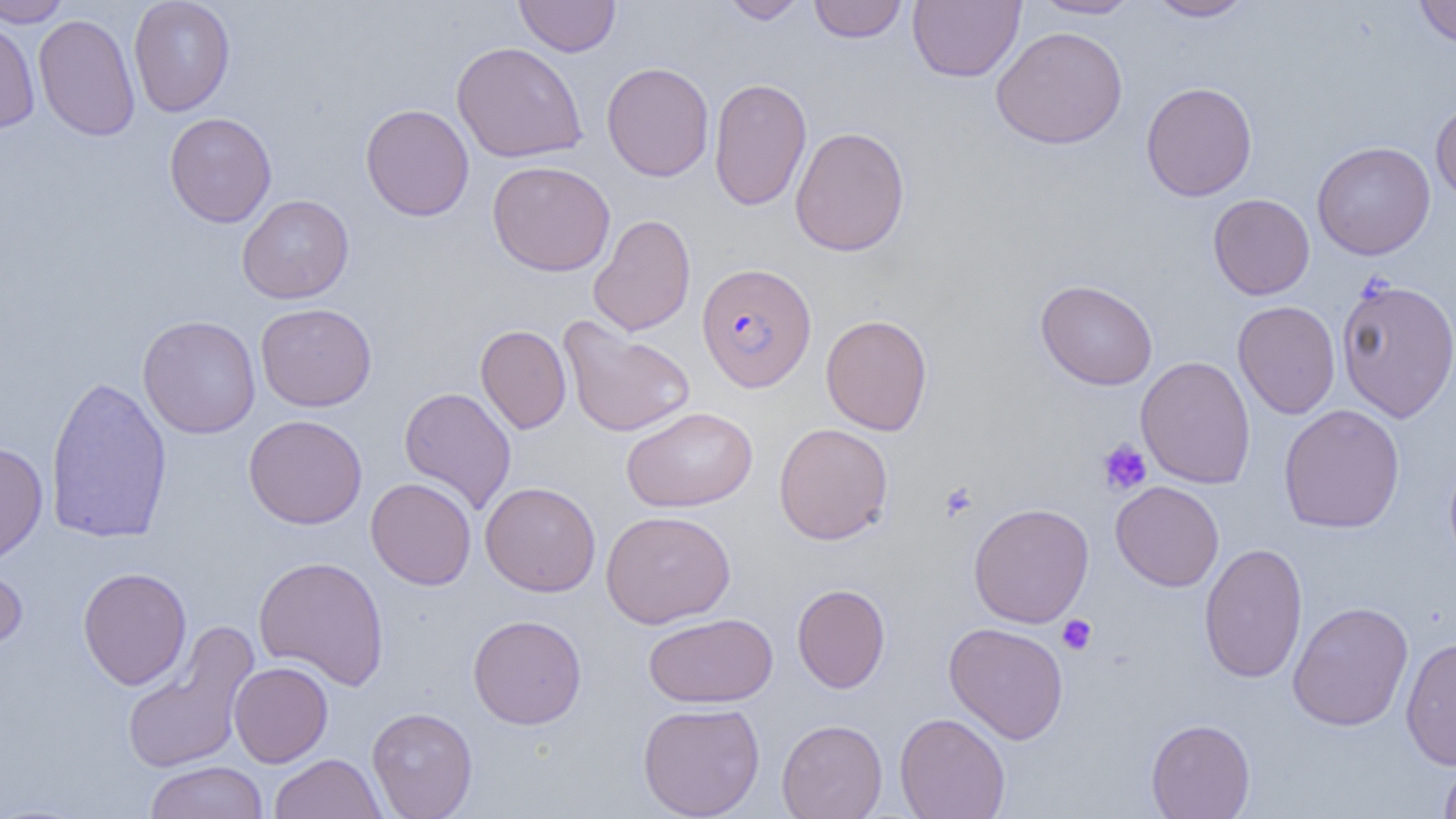

Summary:
  - Coordinate format: approximate bounding boxes as (x1,y1)-(x2,y2) corner pairs in pixels
  - Uninfected red blood cell locations: (0,0)-(72,28), (128,0)-(235,117), (514,0)-(620,57), (719,0)-(809,24), (808,0)-(907,43), (908,0)-(1025,82), (1029,0)-(1140,19), (1145,0)-(1257,21), (1413,0)-(1456,48), (33,13)-(141,142), (0,15)-(40,133), (991,26)-(1128,149), (451,41)-(588,163), (601,62)-(714,181), (709,77)-(811,210), (1140,81)-(1257,201), (1430,99)-(1456,204), (360,103)-(474,221), (164,112)-(277,227), (790,126)-(910,257), (1312,141)-(1435,260), (486,160)-(616,277), (1208,193)-(1315,299), (237,194)-(354,304), (588,214)-(696,336), (1334,278)-(1456,422), (1035,279)-(1158,390), (1233,300)-(1340,419), (255,303)-(377,412), (137,314)-(261,438), (821,314)-(933,435), (558,317)-(696,437), (475,324)-(572,434), (1136,356)-(1256,489), (44,374)-(173,545), (398,386)-(517,514), (1278,404)-(1405,533), (621,406)-(758,513), (243,414)-(367,529), (773,422)-(894,545), (0,442)-(49,564), (1444,454)-(1456,575), (365,477)-(477,590), (480,481)-(601,596), (1110,481)-(1224,591), (968,502)-(1095,628), (600,509)-(736,629), (1199,542)-(1308,684), (252,554)-(390,691), (0,556)-(28,655), (77,567)-(192,690), (792,583)-(891,693), (1288,601)-(1414,731), (643,612)-(778,708), (467,613)-(587,729), (943,622)-(1069,744), (120,623)-(259,775), (1400,636)-(1456,770), (229,661)-(333,767), (638,702)-(765,819), (366,706)-(478,818), (895,712)-(1011,819), (777,718)-(887,819), (1146,718)-(1255,819), (269,752)-(386,818), (1438,756)-(1456,819), (144,760)-(270,819)
  - Plasmodium falciparum-infected red blood cell locations: (697,263)-(816,393)
  - Platelet locations: (1097,438)-(1152,495), (939,481)-(978,522), (1057,615)-(1097,656)
  - Slide-level diagnosis: Plasmodium falciparum
  - Magnification: 1000x
  - Modality: optical microscopy
  - Field of view: one of a larger specimen
  - Image size: 1456×819 pixels
  - Preparation: thin blood film